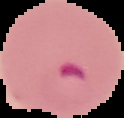

Summary:
  - Image size: 124×118 pixels
  - Preparation: thin blood film
  - Image type: segmented cell region on a black background
  - Malaria status: parasitized